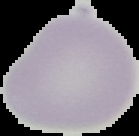

{
  "malaria_status": "uninfected",
  "preparation": "thin blood smear",
  "image_size": "139×136 pixels",
  "image_type": "cell region segmented out of the field of view; surrounding area masked to black"
}